State the preparation type.
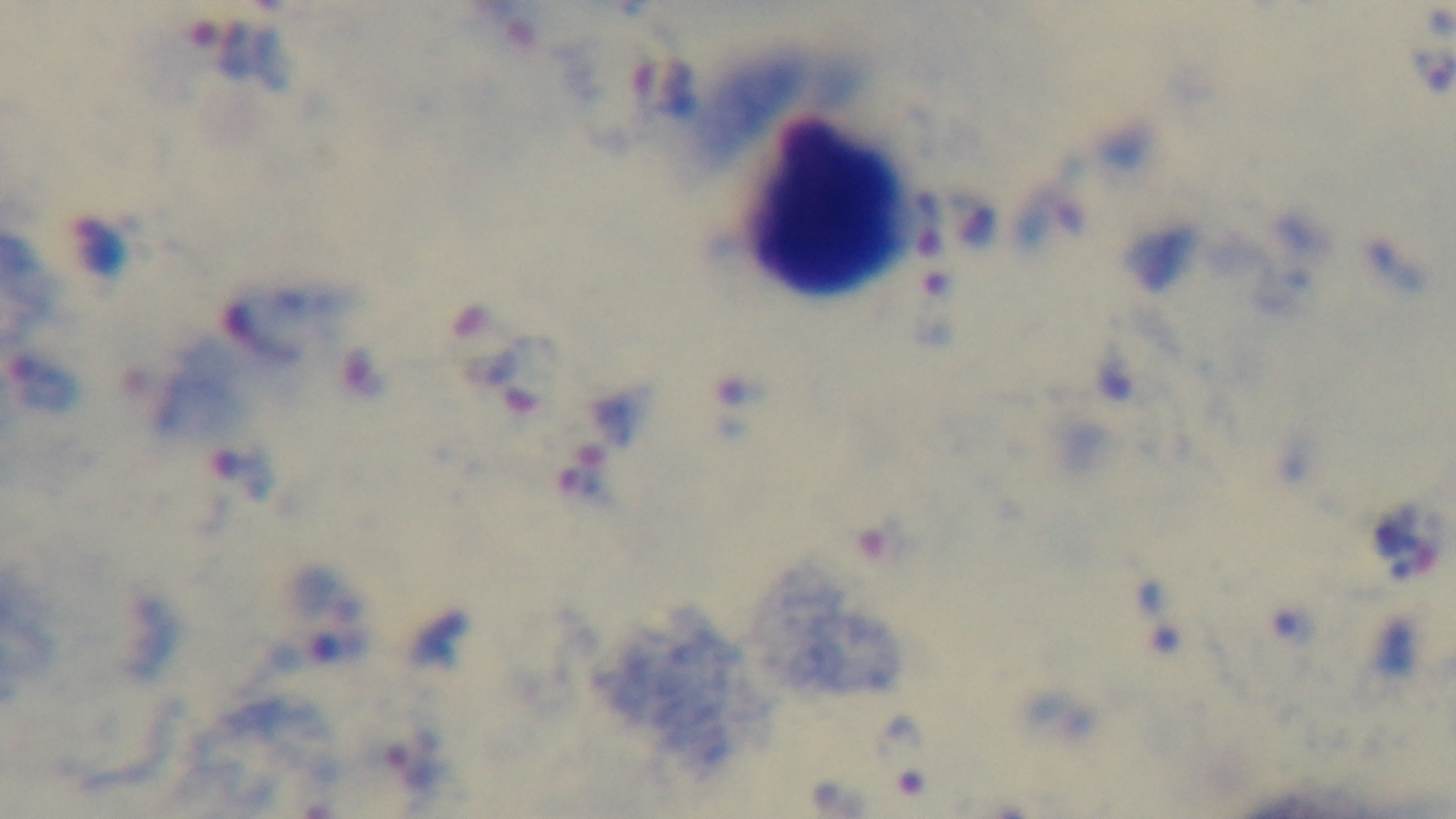
Thick.

capture: mounted 4K digital camera
stain: Giemsa
modality: light microscopy
malaria_status: infected
field_of_view: single
objective: 100x oil immersion